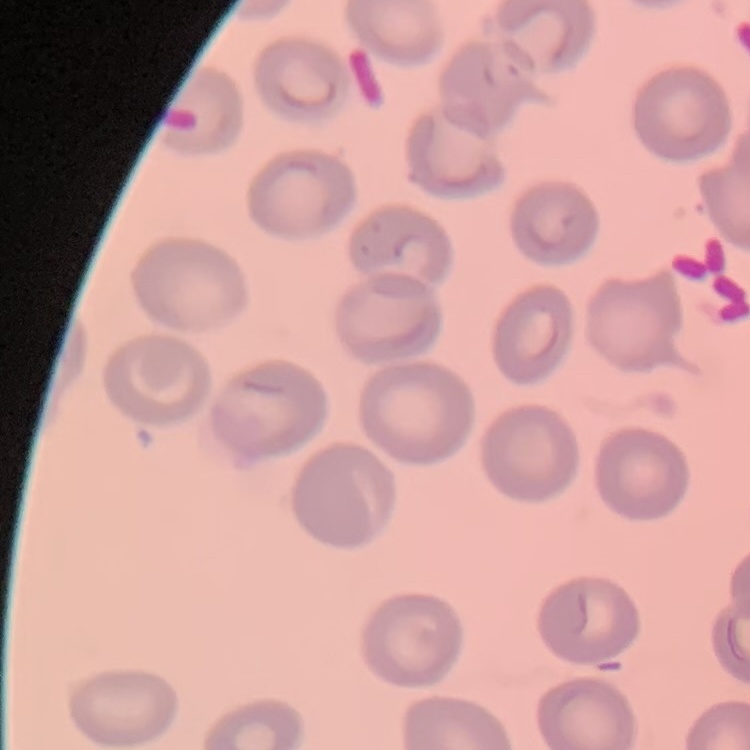

Summary:
  - Red blood cell morphology: no rouleaux formation
  - Preparation: thin blood film
  - Image type: square crop of a larger photomicrograph
  - Stain: Field's or Giemsa